Give the extent of all Plasmodium vivax-infected red blood cells.
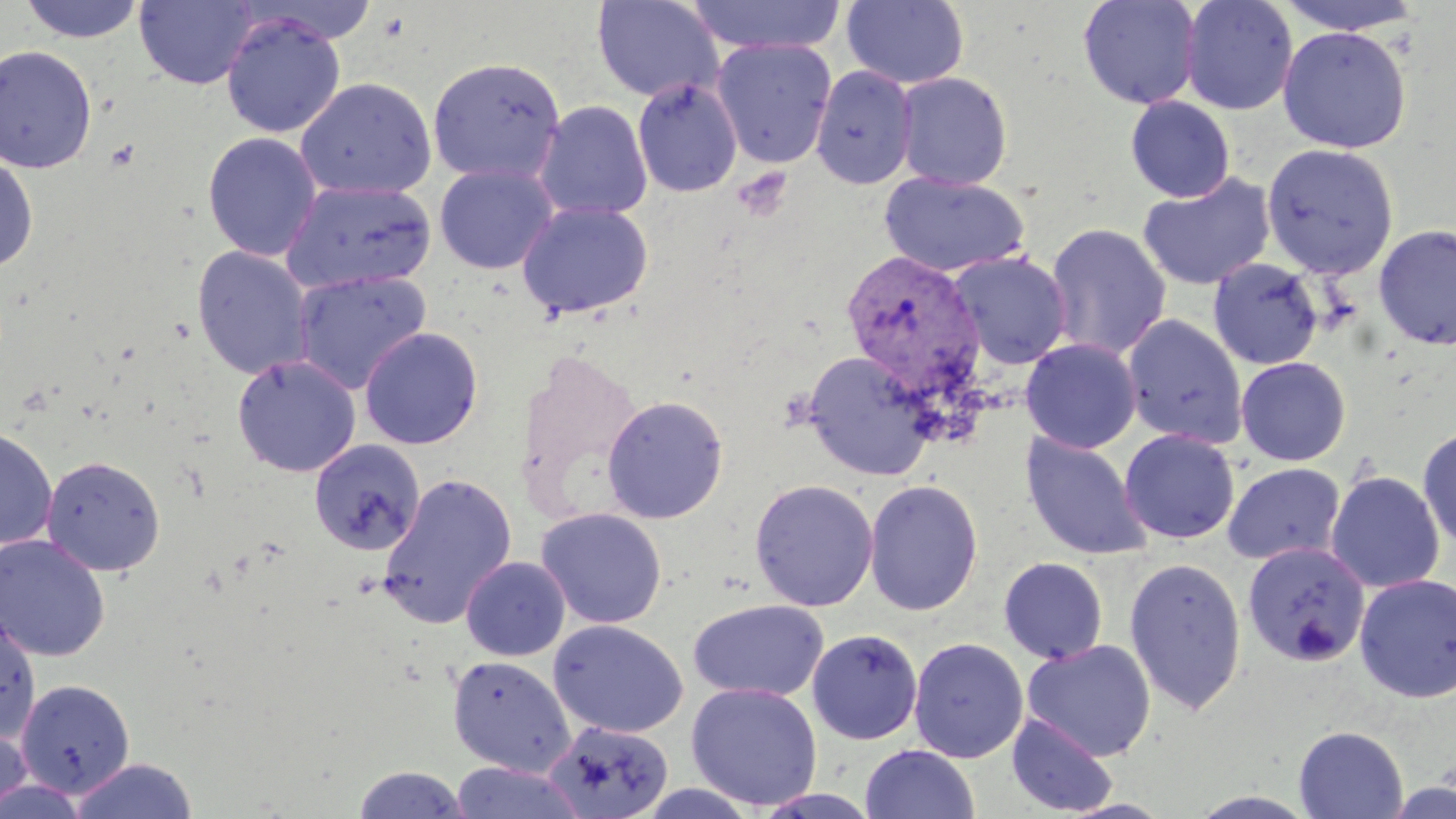
Approximate bounding boxes as (x1,y1)-(x2,y2) corner pairs in pixels.
Plasmodium vivax-infected red blood cells: (840,250)-(986,403).

slide-level diagnosis = Plasmodium vivax
uninfected red blood cell locations = approximate bounding boxes as (x1,y1)-(x2,y2) corner pairs in pixels: (19,0)-(146,44), (134,0)-(257,89), (592,0)-(723,103), (687,0)-(846,55), (842,0)-(970,89), (1077,0)-(1202,109), (1179,0)-(1299,116), (1275,0)-(1428,36), (221,13)-(345,138), (1277,25)-(1412,153), (711,38)-(837,168), (0,44)-(98,174), (427,57)-(566,185), (810,66)-(917,188), (895,72)-(1012,191), (295,78)-(436,199), (633,78)-(742,197), (1125,95)-(1235,203), (535,100)-(652,221), (202,131)-(323,262), (1261,142)-(1399,279), (0,153)-(39,275), (434,164)-(559,275), (879,172)-(1030,277), (1137,172)-(1276,291), (281,179)-(437,295), (516,200)-(653,320), (1045,222)-(1171,360), (1373,223)-(1456,350), (191,246)-(316,381), (947,251)-(1072,370), (1208,258)-(1324,370), (292,270)-(432,394), (1121,314)-(1248,449), (358,326)-(484,450), (1021,338)-(1141,453), (802,349)-(938,481), (232,354)-(362,477), (1235,356)-(1351,466), (602,394)-(729,524), (1417,424)-(1456,552), (0,426)-(58,550), (1119,429)-(1240,544), (1020,433)-(1152,560), (308,439)-(426,556), (41,455)-(165,577), (1223,462)-(1345,566), (1325,470)-(1445,594), (377,473)-(517,627), (749,478)-(879,611), (864,479)-(983,617), (535,507)-(667,629), (0,533)-(111,662), (1242,541)-(1370,668), (460,556)-(571,661), (998,556)-(1108,664), (1123,556)-(1247,715), (1354,573)-(1456,704), (687,598)-(829,702), (0,610)-(41,745), (548,619)-(688,738), (807,628)-(923,745), (909,637)-(1028,763), (1022,640)-(1156,761), (447,655)-(577,777), (16,679)-(135,797), (686,682)-(823,810), (1006,712)-(1118,817), (544,720)-(673,818), (0,721)-(33,816), (1294,725)-(1408,818), (860,744)-(979,819), (69,757)-(199,818), (449,760)-(587,819), (349,765)-(475,818), (0,776)-(90,817), (1384,781)-(1456,819), (634,782)-(760,818), (754,789)-(882,818), (1187,791)-(1320,819)
image size = 1456×819 pixels
modality = optical microscopy
field of view = one of a larger specimen
stain = May-Grünwald-Giemsa
magnification = 1000x
preparation = thin blood film